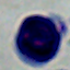

Captured at 1000x magnification. A leukocyte is seen. Photomicrograph.